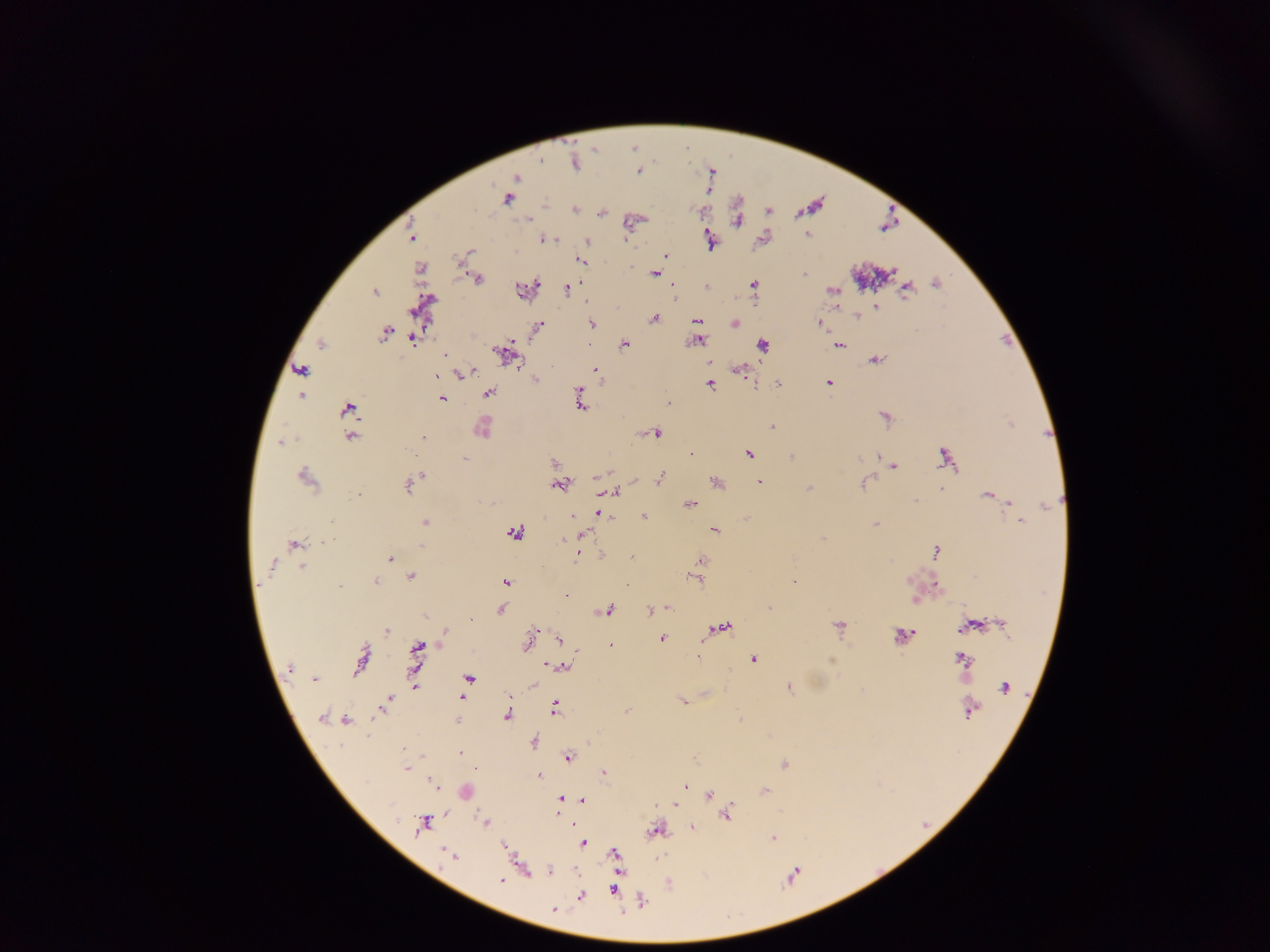 Approximate centers as {x, y} in pixels. Malaria parasite locations: {574, 163}, {638, 172}, {516, 177}, {507, 199}, {575, 210}, {600, 213}, {806, 235}, {411, 237}, {627, 238}, {553, 239}, {544, 240}, {587, 241}, {709, 242}, {469, 252}, {665, 256}, {581, 262}, {655, 274}, {804, 275}, {478, 278}, {935, 283}, {754, 285}, {567, 289}, {906, 289}, {518, 290}, {832, 291}, {374, 292}, {876, 307}, {857, 315}, {654, 318}, {696, 320}, {819, 322}, {735, 323}, {591, 324}, {538, 326}, {384, 334}, {413, 340}, {698, 341}, {321, 345}, {590, 345}, {624, 345}, {762, 345}, {839, 345}, {501, 352}, {445, 355}, {875, 360}, {709, 362}, {301, 370}, {595, 370}, {740, 370}, {472, 372}, {437, 374}, {461, 374}, {535, 380}, {778, 383}, {828, 383}, {710, 384}, {489, 393}, {580, 394}, {301, 397}, {442, 398}, {668, 403}, {580, 405}, {347, 408}, {885, 417}, {772, 427}, {481, 429}, {656, 434}, {350, 436}, {423, 437}, {281, 443}, {691, 453}, {748, 454}, {879, 456}, {791, 457}, {944, 457}, {464, 459}, {554, 463}, {893, 466}, {421, 476}, {598, 476}, {305, 477}, {661, 477}, {716, 482}, {759, 482}, {863, 483}, {557, 485}, {408, 486}, {810, 488}, {941, 489}, {613, 492}, {359, 493}, {988, 496}, {915, 501}, {1011, 503}, {690, 504}, {1045, 506}, {600, 514}, {572, 517}, {644, 517}, {746, 518}, {331, 522}, {1021, 522}, {425, 523}, {874, 525}, {715, 530}, {514, 533}, {583, 535}, {822, 538}, {564, 539}, {326, 541}, {294, 545}, {421, 545}, {935, 552}, {576, 555}, {631, 558}, {390, 559}, {701, 561}, {271, 565}, {302, 567}, {411, 576}, {696, 580}, {793, 581}, {375, 582}, {506, 582}, {935, 585}, {340, 586}, {565, 596}, {769, 608}, {501, 609}, {667, 609}, {608, 610}, {651, 610}, {424, 617}, {470, 619}, {1002, 623}, {839, 626}, {967, 627}, {725, 628}, {387, 630}, {445, 632}, {901, 635}, {661, 639}, {558, 640}, {528, 641}, {611, 645}, {417, 650}, {698, 655}, {361, 659}, {754, 659}, {962, 659}, {290, 668}, {562, 668}, {469, 678}, {315, 680}, {414, 685}, {532, 686}, {1004, 686}, {788, 687}, {463, 696}, {387, 702}, {683, 702}, {555, 709}, {970, 711}, {627, 712}, {507, 716}, {320, 718}, {345, 720}, {458, 720}, {534, 742}, {403, 749}, {460, 753}, {569, 758}, {784, 764}, {405, 768}, {604, 773}, {539, 777}, {431, 783}, {685, 785}, {680, 789}, {765, 790}, {710, 795}, {561, 799}, {582, 800}, {676, 805}, {728, 815}, {485, 823}, {422, 824}, {692, 828}, {655, 830}, {772, 838}, {583, 843}, {504, 846}, {615, 854}, {450, 855}, {550, 871}, {501, 880}, {614, 889}, {580, 896}, {554, 909}. Mobile-phone photograph taken through the microscope. Image is 1270×952 pixels. Thick blood smear. Single field of view. Collected in Ghana.